Report the malaria status of this cell.
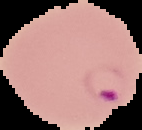
It is parasitized.

Image is 142×130 pixels. From a thin blood film. The area outside the segmented cell region is set to black.